State which parasite is depicted.
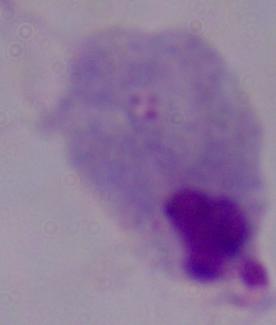
This is a trichomonad.

Captured at 1000x magnification. Photomicrograph.